State which parasite is depicted.
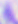
This is Toxoplasma gondii.

Summary:
  - Magnification: 400x
  - Modality: photomicrograph